Comment on the morphology of the red blood cells.
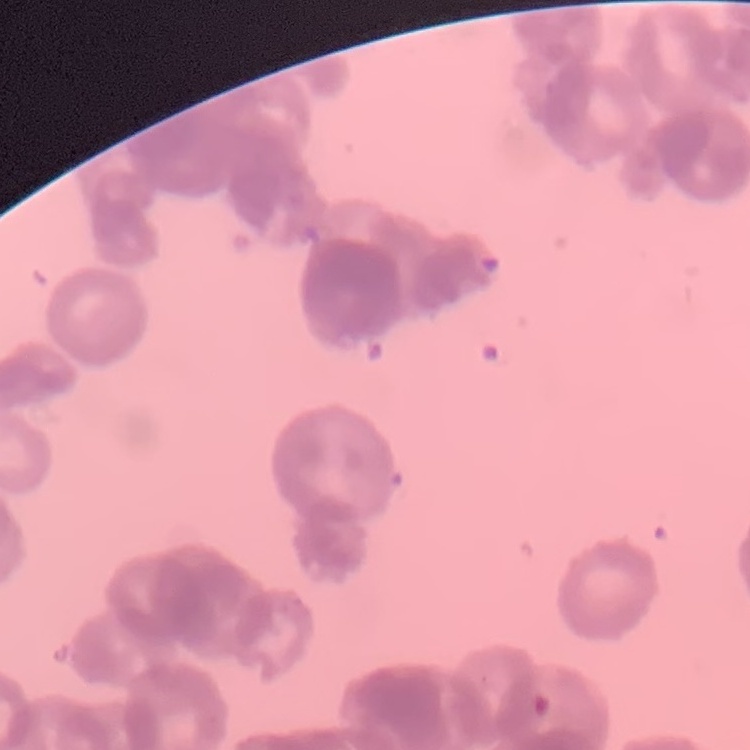
Rouleaux formation.

Stained with either Field's or Giemsa. Thin peripheral smear. One tile cut from a larger photomicrograph.